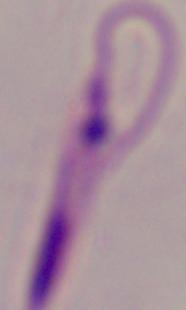
Photomicrograph. A Leishmania parasite is shown. Captured at 1000x magnification.